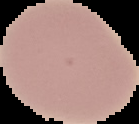

Image is 139×124 pixels. Result: no Plasmodium parasites seen. From a thin blood film. Cell region segmented out of the field of view; the surrounding area is masked to black.